Outline each P. falciparum parasite and classify it by life-cycle stage.
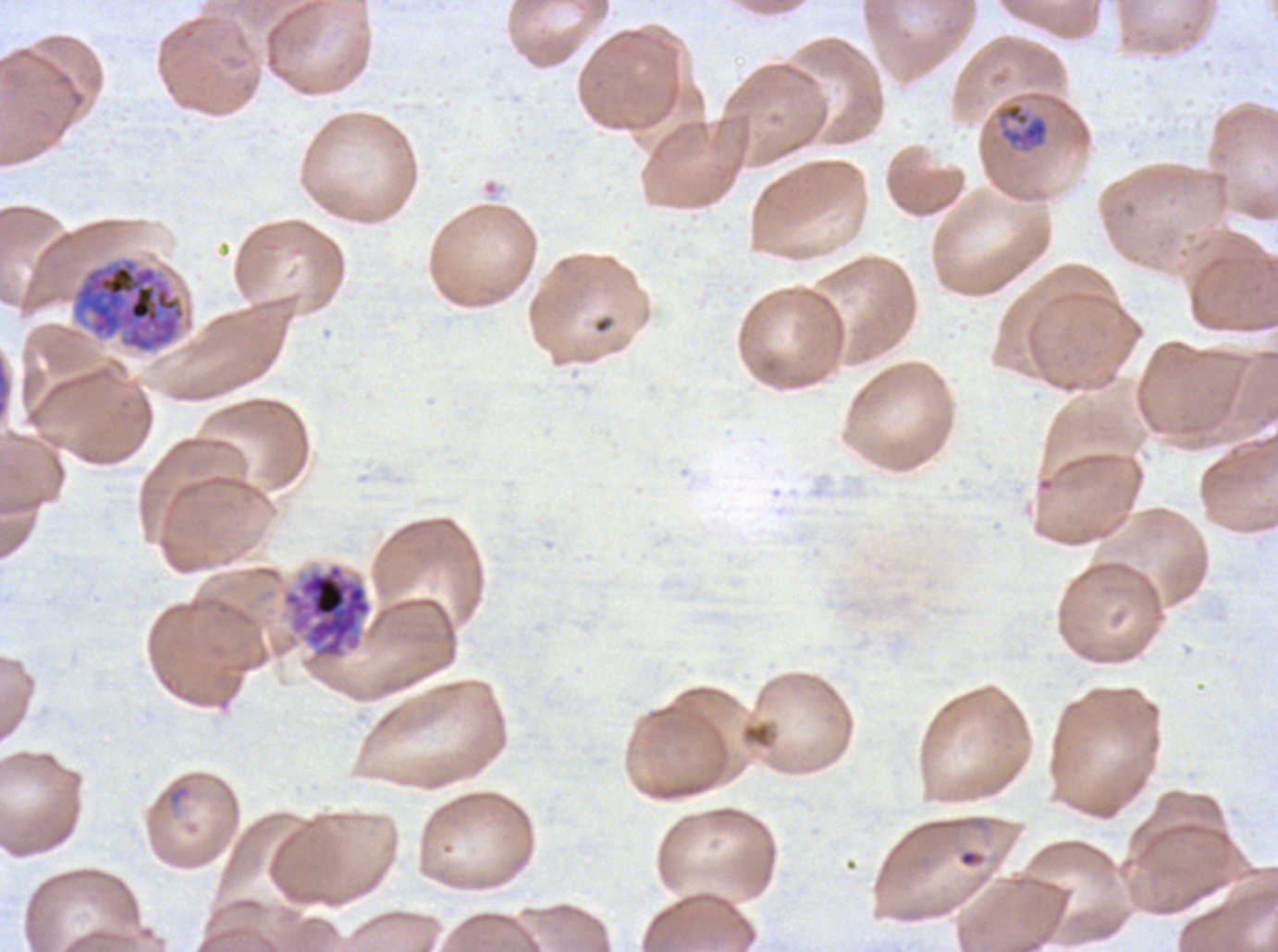
Approximate bounding boxes as [x1, y1, x2, y2] in pixels.
Rings: [169, 785, 189, 802].
Mid trophozoites: [996, 102, 1050, 153].
Late schizonts: [70, 257, 187, 354], [280, 562, 374, 662].
No late-ring/early-trophozoite forms, late trophozoites, early schizonts, segmenters, or gametocytes observed.

A sub-image separated from a larger composite. Life-cycle stages observed: ring, mid trophozoite, late schizont. P. falciparum from a patient in The Gambia, cultured ex vivo for 24 to 48 hours. Image is 1278×952 pixels. Thin blood smear. Giemsa stain.